Report the malaria status of this cell.
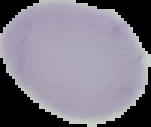
It is uninfected.

preparation = thin blood film
image size = 151×127 pixels
image type = cell region segmented out of the field of view; surrounding area masked to black